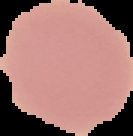
Summary:
  - Image size: 133×136 pixels
  - Result: no malaria parasites seen
  - Preparation: thin blood smear
  - Image type: segmented cell region on a black background